Locate every Plasmodium malariae-infected red blood cell.
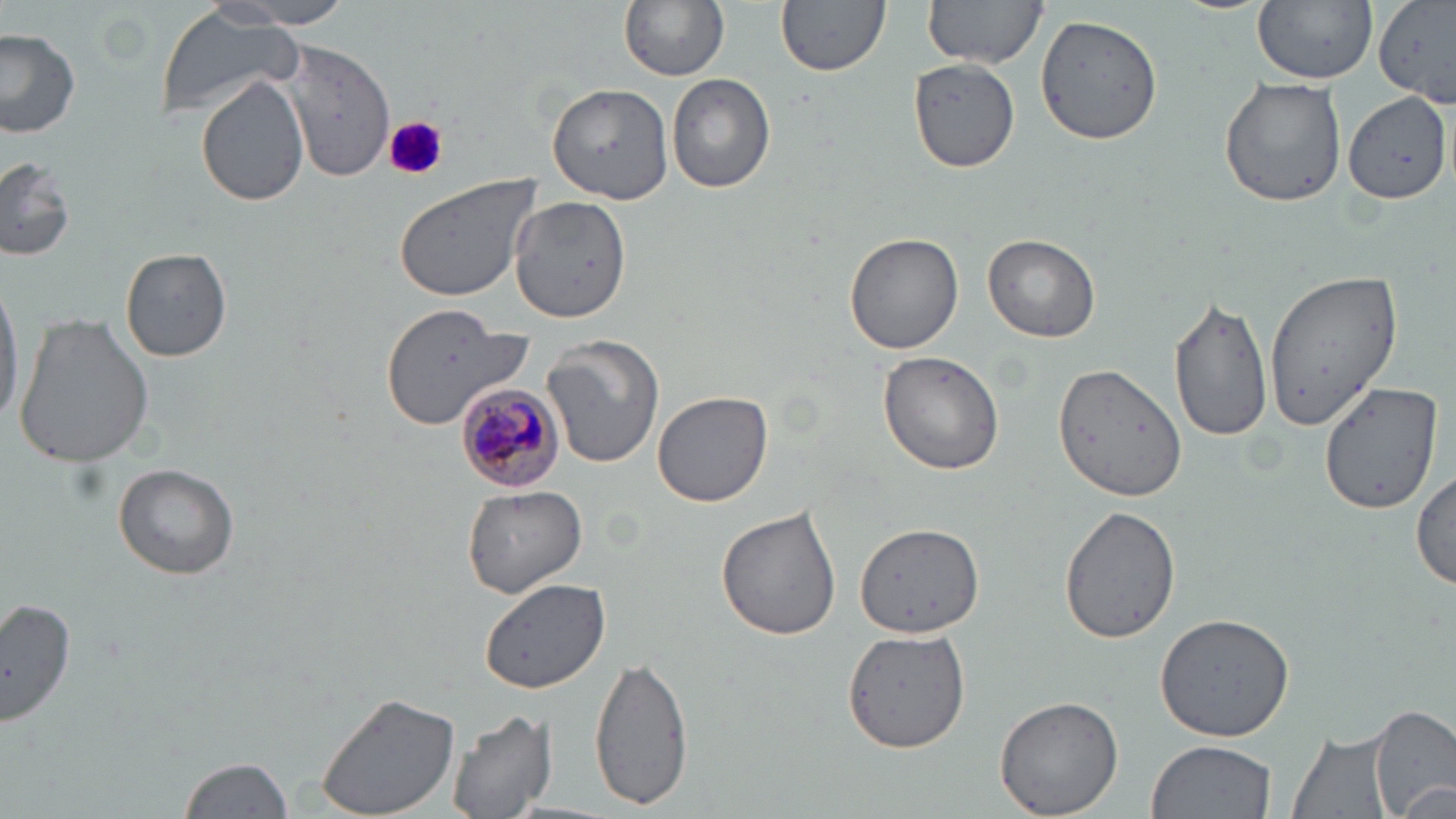
Approximate bounding boxes as (x1, y1, x2, y2) in pixels.
Plasmodium malariae-infected red blood cells: (455, 382, 567, 496).

Uninfected red blood cell locations: (622, 0, 728, 82), (775, 0, 889, 76), (1253, 0, 1377, 85), (217, 1, 357, 27), (919, 1, 1048, 69), (155, 5, 304, 121), (1033, 12, 1165, 146), (0, 27, 79, 138), (278, 39, 395, 181), (910, 59, 1023, 171), (666, 72, 776, 194), (197, 75, 311, 207), (1216, 75, 1349, 209), (547, 82, 674, 203), (1343, 90, 1452, 203), (0, 158, 74, 264), (391, 171, 545, 302), (509, 195, 633, 323), (844, 232, 964, 355), (983, 233, 1101, 343), (120, 247, 233, 361), (1264, 270, 1407, 429), (0, 275, 26, 427), (1169, 294, 1274, 444), (12, 312, 155, 469), (378, 312, 537, 430), (541, 336, 666, 470), (878, 349, 1005, 475), (1053, 362, 1186, 503), (1319, 380, 1443, 515), (653, 389, 774, 506), (112, 461, 241, 579), (1413, 465, 1455, 592), (463, 485, 586, 598), (1059, 504, 1181, 644), (715, 505, 842, 642), (853, 521, 986, 640), (477, 576, 610, 695), (0, 596, 77, 730), (1155, 611, 1297, 742), (841, 626, 970, 754), (588, 651, 696, 810), (315, 691, 463, 819), (994, 694, 1125, 818), (1370, 705, 1454, 819), (443, 707, 558, 818), (1286, 726, 1397, 819), (1146, 741, 1276, 819), (179, 754, 294, 819). Platelet locations: (383, 114, 447, 182). Slide-level diagnosis: Plasmodium malariae. Optical microscopy. Captured at 1000x magnification. May-Grünwald-Giemsa stain. Thin blood film. Image is 1456×819 pixels. One field of a larger specimen.